Give the position of every malaria parasite.
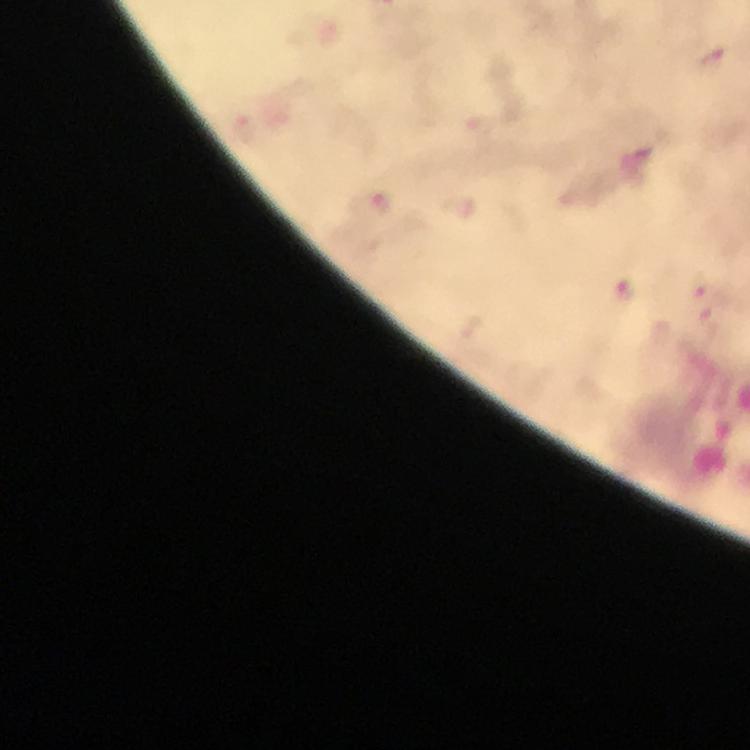
Approximate centers as {x, y} in pixels.
Malaria parasites: {713, 58}.

Summary:
  - Capture: smartphone camera through the microscope
  - Cropped from: a single field of view
  - Context: from a diagnostic examination for malaria
  - Preparation: thick blood film
  - Magnification: 100x
  - Immersion oil: applied
  - Stain: Giemsa
  - Image size: 750×750 pixels